Point out each Plasmodium parasite.
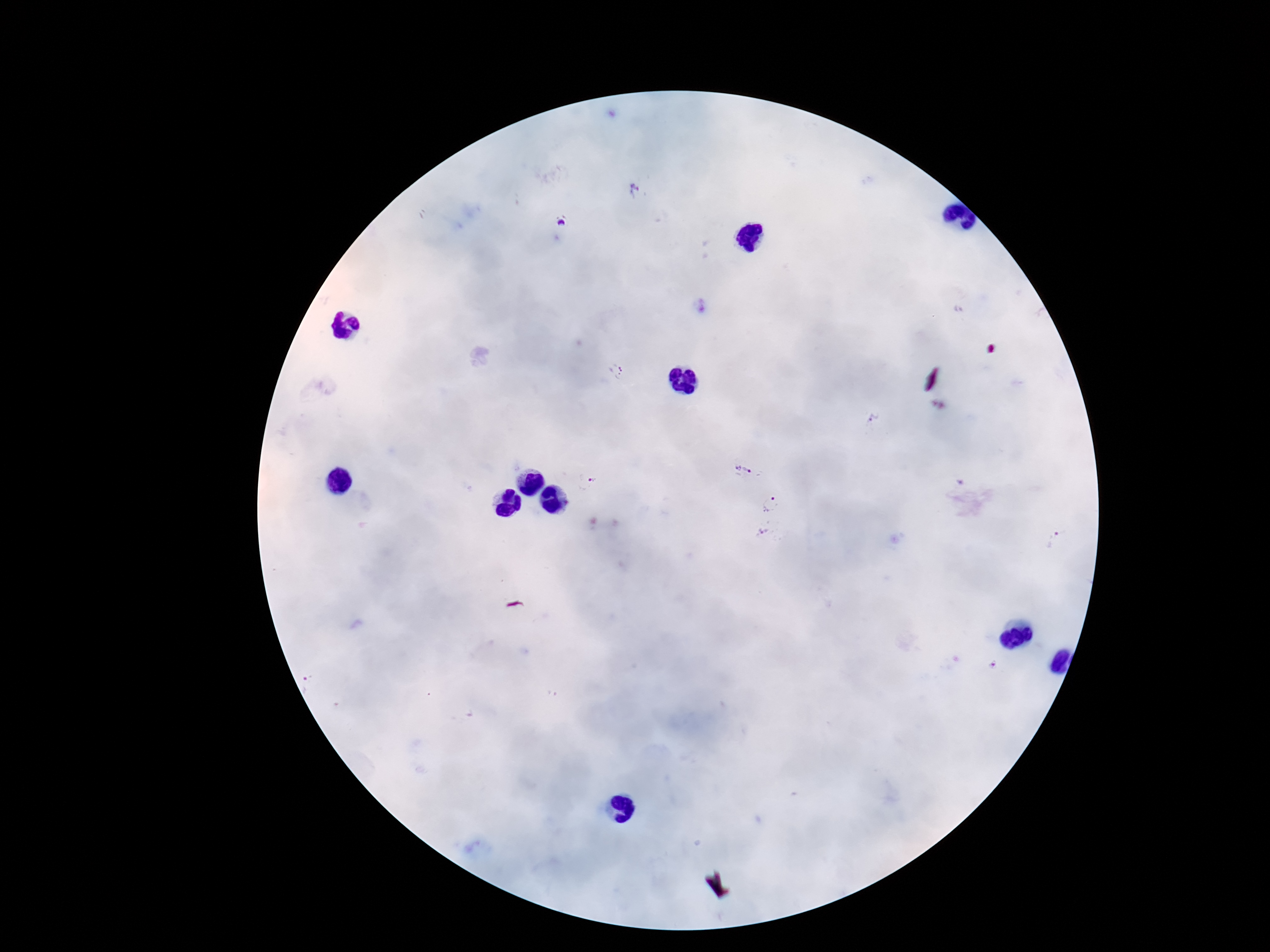

Approximate centers as [x, y] in pixels.
Plasmodium parasites: [615, 372], [875, 418], [742, 470], [594, 480], [770, 505].

Summary:
  - Preparation: thick blood smear
  - Magnification: 100x
  - Capture: smartphone camera through the microscope eyepiece
  - Stain: Giemsa
  - Patient malaria status: infected
  - Image size: 1270×952 pixels
  - Field of view: one from this slide